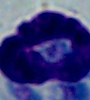 Captured at 1000x magnification. A leukocyte is seen. Micrograph.